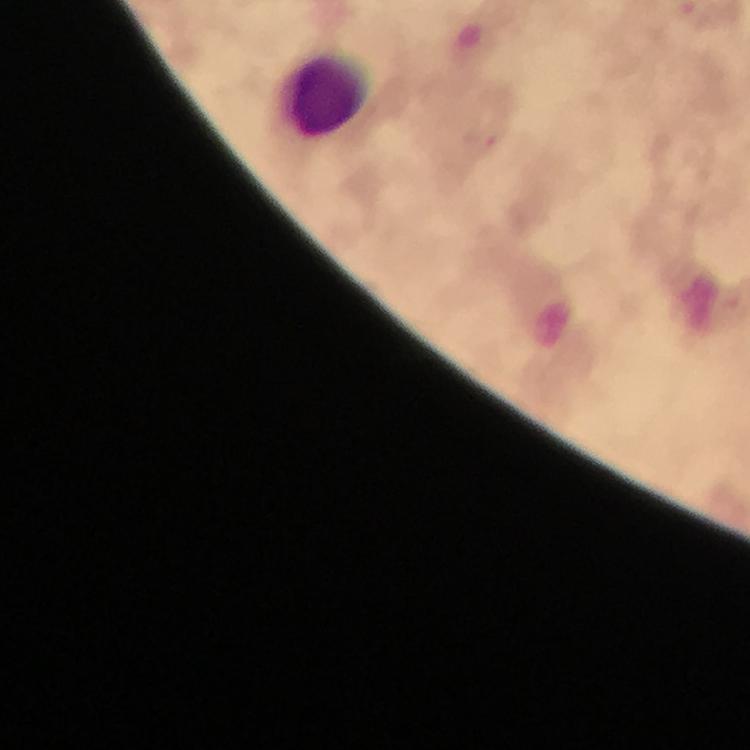
Approximate object centers, in pixels from the top-left corner.
Summary:
  - Leukocyte locations: (x=324, y=92)
  - Context: from a diagnostic examination for malaria
  - Immersion oil: used
  - Preparation: thick smear
  - Magnification: 100x
  - Capture: smartphone photograph through a microscope
  - Plasmodium parasites: none seen
  - Image size: 750×750 pixels
  - Stain: Giemsa
  - Cropped from: a single field of view